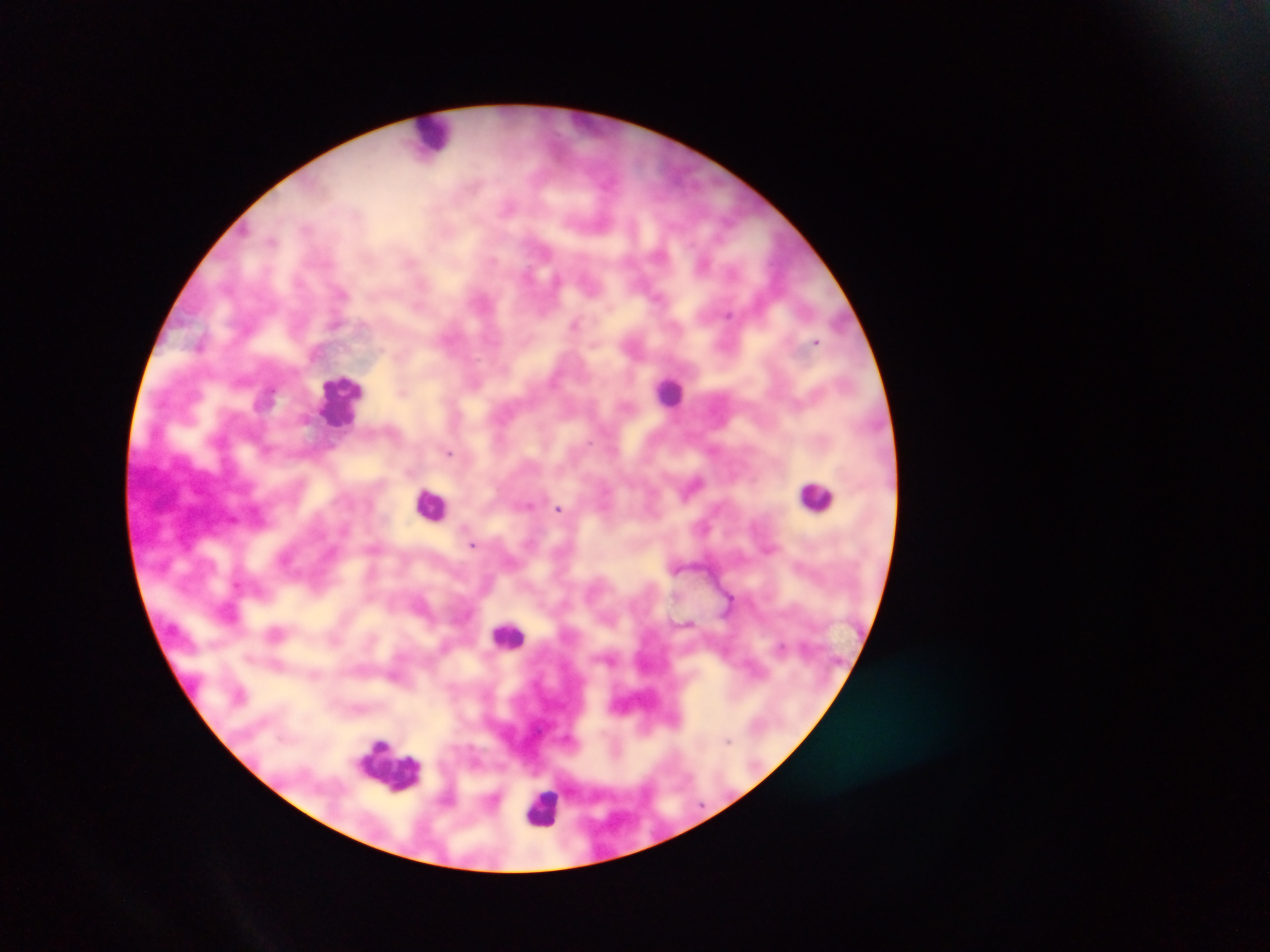
Plasmodium parasite locations = approximate centers as x y in pixels: 703 263; 576 324; 816 341; 403 390; 305 419; 449 452; 694 482; 559 508; 472 544; 676 568; 276 632; 782 647; 728 741
image size = 1270×952 pixels
field of view = single
leukocyte locations = approximate centers as x y in pixels: 433 135; 670 391; 342 401; 816 496; 432 504; 509 635; 389 763; 543 809
country = Ghana
capture = mobile-phone photograph through a microscope
preparation = thick blood film